Locate every P. falciparum parasite and identify its life-cycle stage.
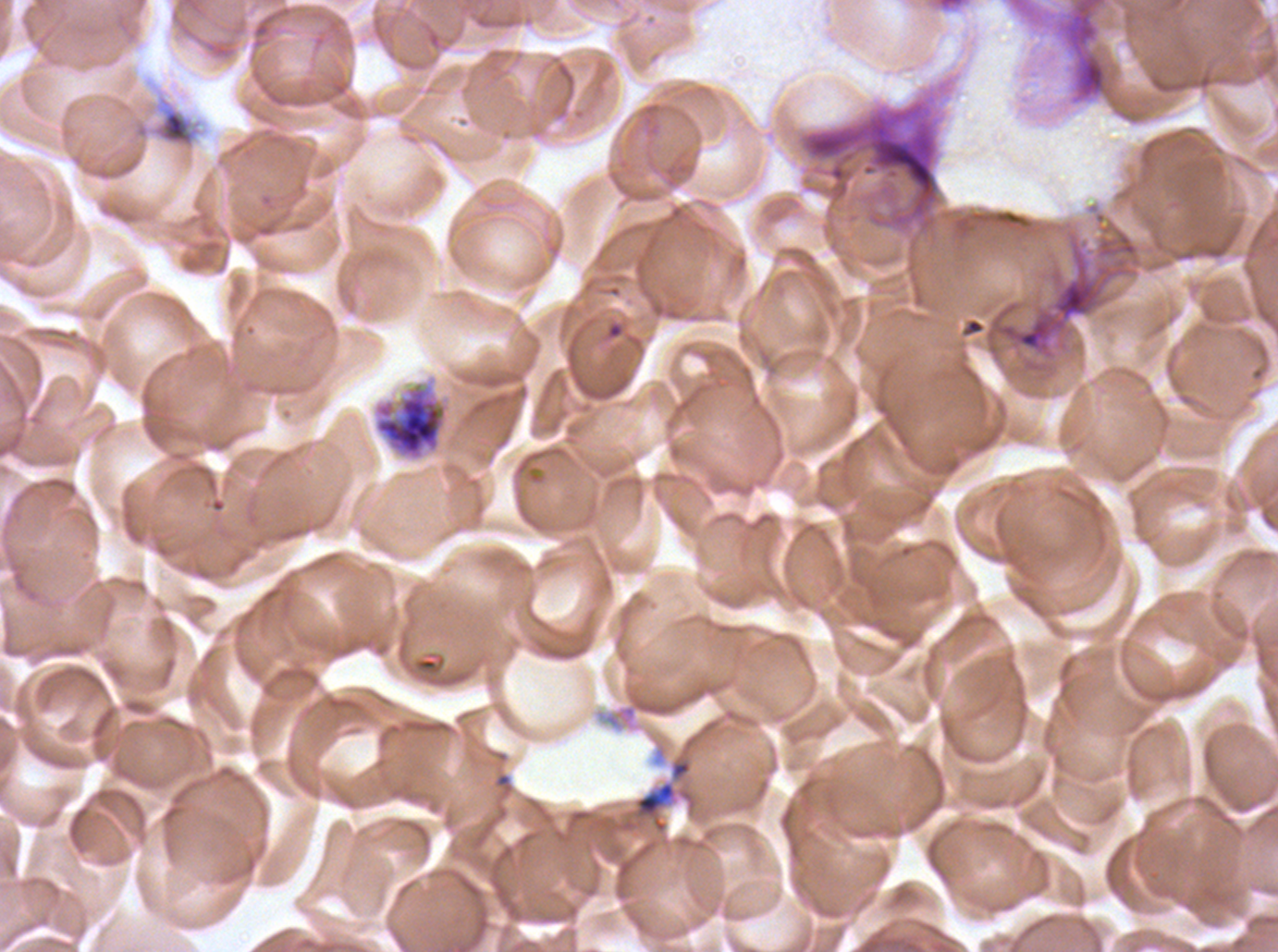
Approximate bounding boxes as [x1, y1, x2, y2] in pixels.
Early schizonts: [372, 380, 451, 462].
No rings, late-ring/early-trophozoite forms, mid trophozoites, late trophozoites, late schizonts, segmenters, or gametocytes observed.

preparation: thin blood film
debris_locations: 'approximate bounding boxes as [x1, y1, x2, y2] in pixels: [1051, 0, 1122, 108], [798, 92, 943, 237], [129, 93, 203, 151], [985, 240, 1127, 341], [633, 780, 679, 835]'
specimen: P. falciparum from a patient in The Gambia, cultured ex vivo for 24 to 48 hours
stain: Giemsa
image_size: 1278×952 pixels
field_of_view: one sub-image of a larger composite